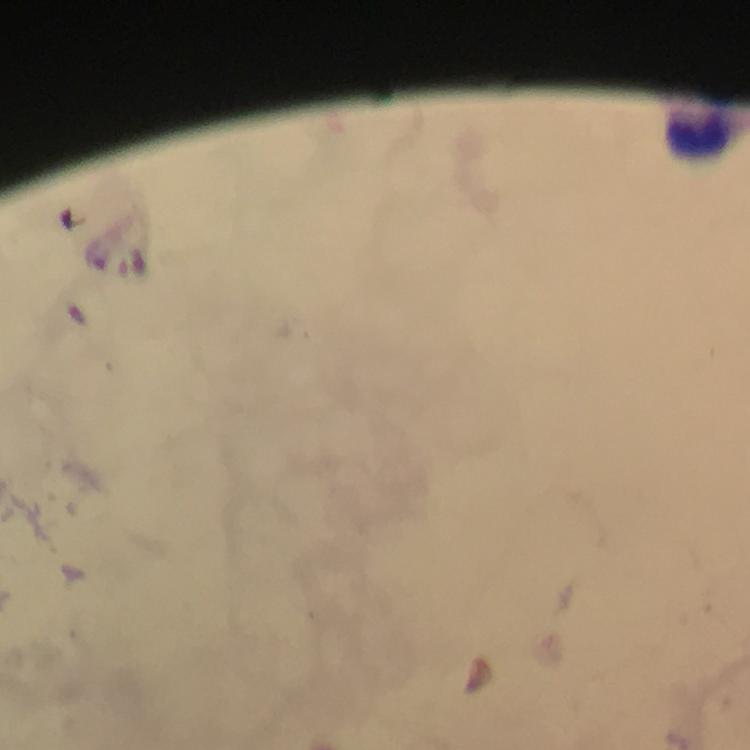
Approximate centers as (x, y) in pixels. Leukocyte locations: (700, 133). Plasmodium parasites: none detected. At 100x magnification. Cropped region of a single field of view. Image is 750×750 pixels. Giemsa-stained preparation. Photographed with a smartphone mounted on the microscope. Thick blood film. Immersion oil was used. From a diagnostic examination for malaria.